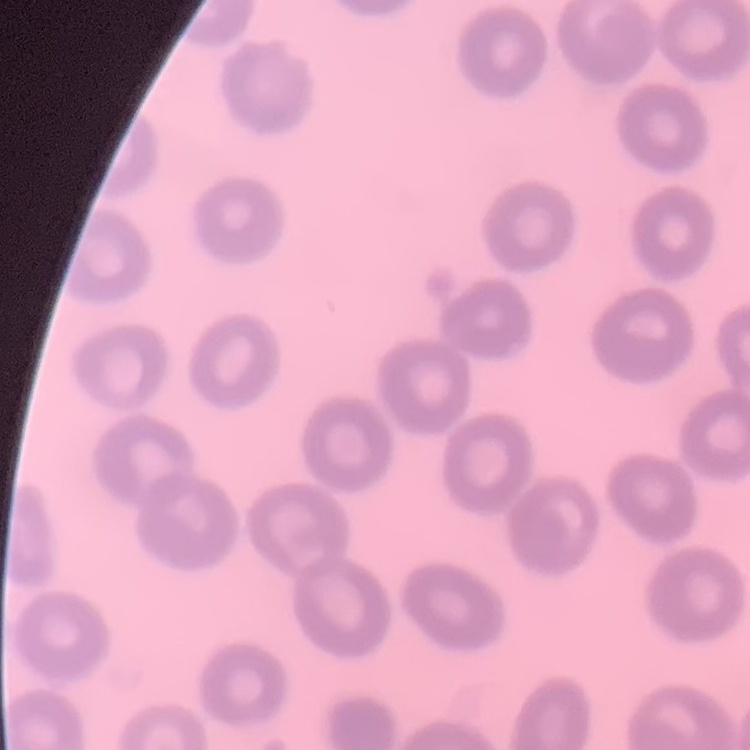

Summary:
  - Red blood cell morphology: no rouleaux formation
  - Stain: Field's or Giemsa
  - Image type: one tile cut from a larger photomicrograph
  - Preparation: thin blood film